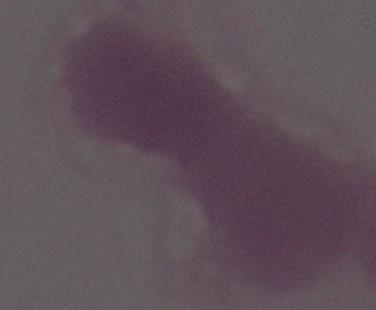

identification: red blood cell
modality: photomicrograph
magnification: 1000x